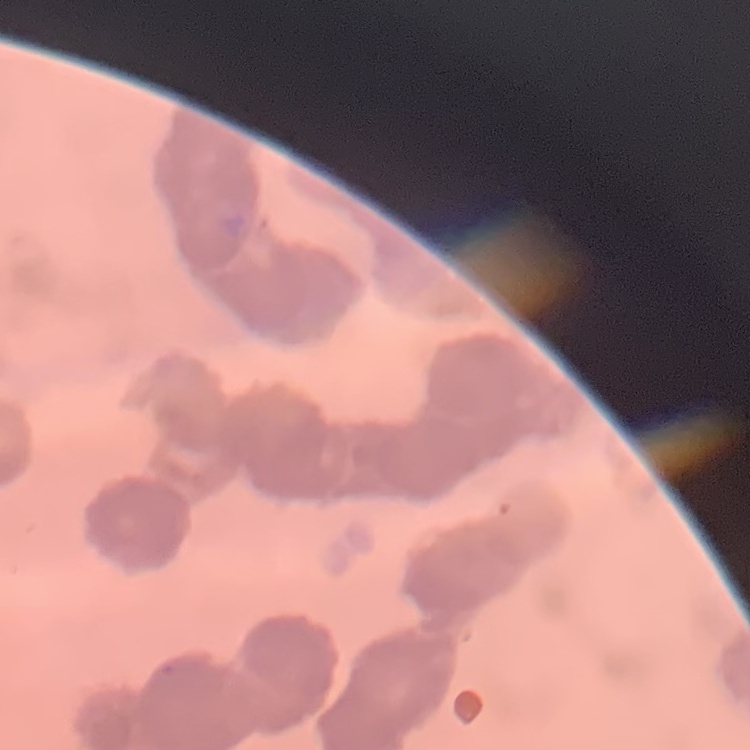
{
  "erythrocyte_morphology": "rouleaux formation",
  "image_type": "one tile cut from a larger photomicrograph",
  "stain": "Field's or Giemsa",
  "preparation": "thin peripheral smear"
}